Outline each blood parasite and name the species.
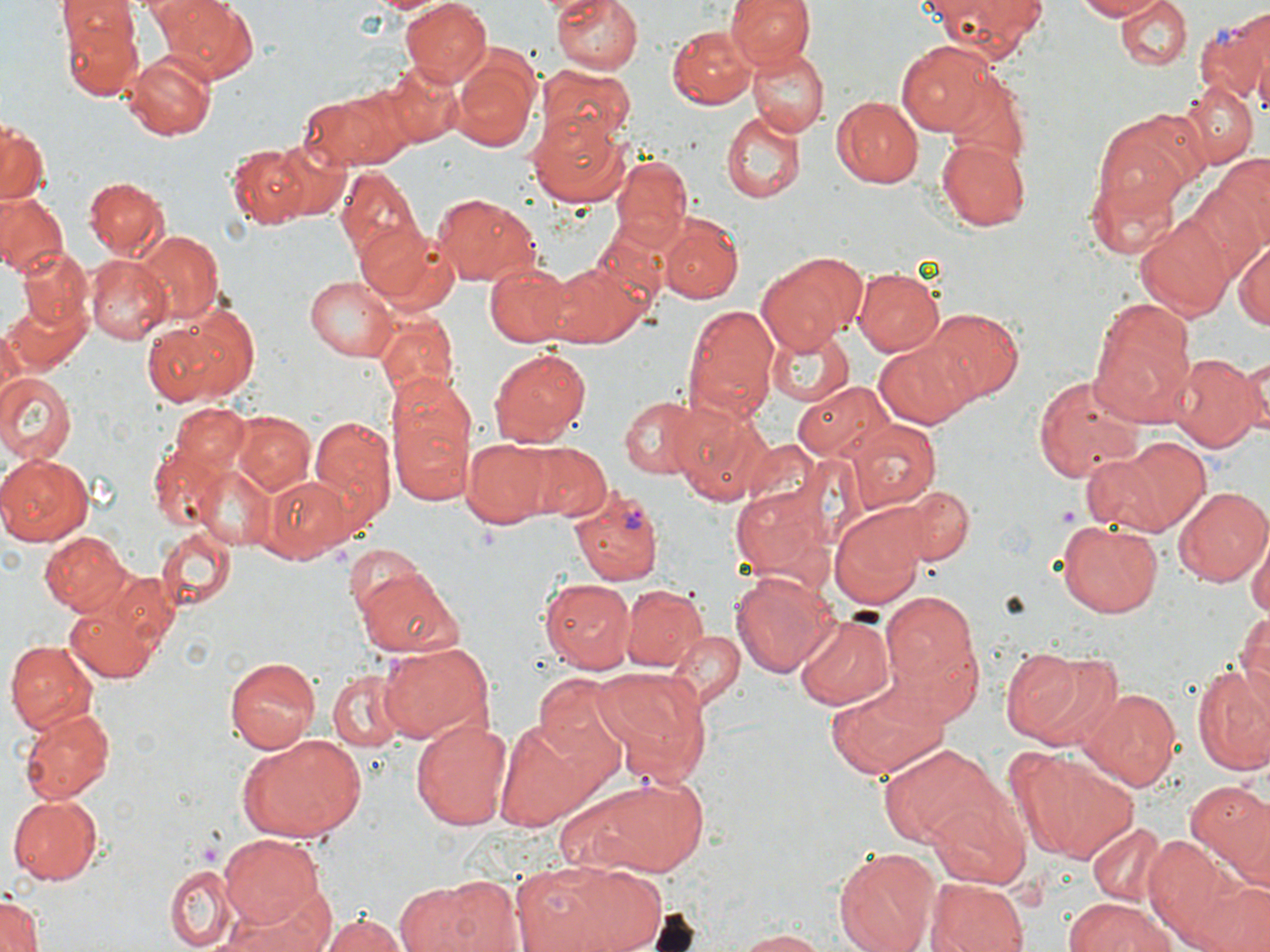

Approximate bounding boxes as [x1, y1, x2, y2] in pixels.
Plasmodium vivax-infected red blood cells: [1195, 13, 1270, 108], [569, 486, 663, 586].
No Plasmodium falciparum, Plasmodium ovale, Plasmodium malariae, Babesia divergens, or Trypanosoma brucei observed.

slide-level diagnosis = Plasmodium vivax
image size = 1270×952 pixels
stain = May-Grünwald-Giemsa
field of view = single
modality = light microscopy
preparation = thin blood smear
platelet locations = approximate bounding boxes as [x1, y1, x2, y2] in pixels: [1056, 504, 1080, 524]
uninfected red blood cell locations = approximate bounding boxes as [x1, y1, x2, y2] in pixels: [51, 0, 210, 89], [152, 0, 255, 84], [398, 0, 492, 85], [549, 0, 643, 75], [725, 0, 813, 70], [916, 0, 1048, 56], [1071, 0, 1168, 21], [1115, 0, 1191, 73], [56, 2, 139, 52], [675, 8, 819, 91], [62, 15, 144, 100], [667, 25, 755, 108], [896, 40, 1002, 134], [747, 46, 828, 139], [451, 49, 540, 155], [120, 51, 216, 142], [362, 57, 463, 150], [536, 65, 635, 148], [943, 76, 1031, 168], [1178, 79, 1257, 166], [302, 85, 410, 169], [832, 95, 925, 189], [1095, 108, 1208, 216], [719, 110, 808, 203], [524, 113, 629, 208], [0, 120, 47, 207], [268, 134, 353, 222], [937, 138, 1034, 230], [226, 143, 312, 228], [610, 153, 694, 254], [1189, 157, 1270, 276], [336, 166, 421, 267], [1088, 167, 1185, 264], [81, 176, 169, 259], [0, 191, 67, 277], [432, 191, 543, 288], [1135, 213, 1234, 319], [659, 214, 744, 302], [357, 219, 458, 314], [135, 229, 223, 324], [1233, 237, 1270, 334], [16, 246, 92, 330], [757, 250, 868, 352], [547, 253, 657, 348], [88, 257, 169, 342], [484, 261, 577, 347], [852, 267, 943, 356], [304, 275, 399, 364], [6, 291, 91, 378], [140, 295, 261, 409], [1091, 296, 1199, 423], [682, 302, 779, 422], [922, 308, 1025, 402], [375, 315, 459, 405], [766, 326, 854, 404], [0, 328, 24, 405], [875, 339, 975, 428], [486, 347, 590, 448], [1169, 353, 1262, 452], [1230, 353, 1269, 443], [0, 373, 75, 464], [1031, 374, 1144, 487], [386, 376, 477, 510], [793, 381, 896, 464], [620, 395, 704, 478], [669, 396, 773, 506], [152, 405, 257, 532], [232, 413, 317, 496], [307, 414, 393, 528], [849, 421, 939, 511], [1095, 435, 1213, 538], [462, 436, 551, 527], [513, 440, 609, 521], [0, 453, 94, 546], [197, 467, 278, 551], [261, 474, 352, 564], [732, 482, 831, 580], [1174, 485, 1270, 586], [893, 487, 973, 566], [830, 506, 927, 607], [1055, 520, 1165, 617], [155, 524, 237, 612], [40, 530, 132, 615], [1248, 540, 1269, 626], [343, 544, 430, 618], [352, 564, 465, 660], [109, 570, 178, 644], [731, 571, 839, 678], [539, 577, 636, 674], [618, 582, 707, 673], [881, 594, 978, 691], [63, 595, 162, 683], [1233, 609, 1270, 714], [795, 612, 896, 713], [875, 625, 985, 730], [667, 630, 743, 712], [375, 638, 495, 743], [5, 639, 100, 736], [1000, 647, 1098, 742], [224, 654, 320, 753], [1191, 663, 1270, 777], [595, 665, 712, 781], [326, 667, 411, 750], [534, 674, 630, 772], [826, 683, 944, 779], [1082, 688, 1182, 793], [19, 707, 115, 802], [410, 718, 512, 830], [493, 724, 592, 826], [239, 735, 367, 841], [876, 741, 1006, 849], [1005, 746, 1137, 865], [554, 773, 709, 878], [1186, 781, 1270, 887], [8, 791, 102, 881], [929, 800, 1029, 888], [1088, 821, 1166, 907], [220, 833, 323, 927], [1143, 834, 1256, 952], [832, 844, 941, 952], [512, 860, 670, 952], [166, 863, 240, 950], [1189, 875, 1269, 952], [394, 877, 502, 952], [927, 877, 1030, 952], [0, 892, 45, 950], [221, 896, 330, 952], [1062, 897, 1182, 952], [318, 912, 410, 952], [733, 929, 833, 951]
magnification = 1000x